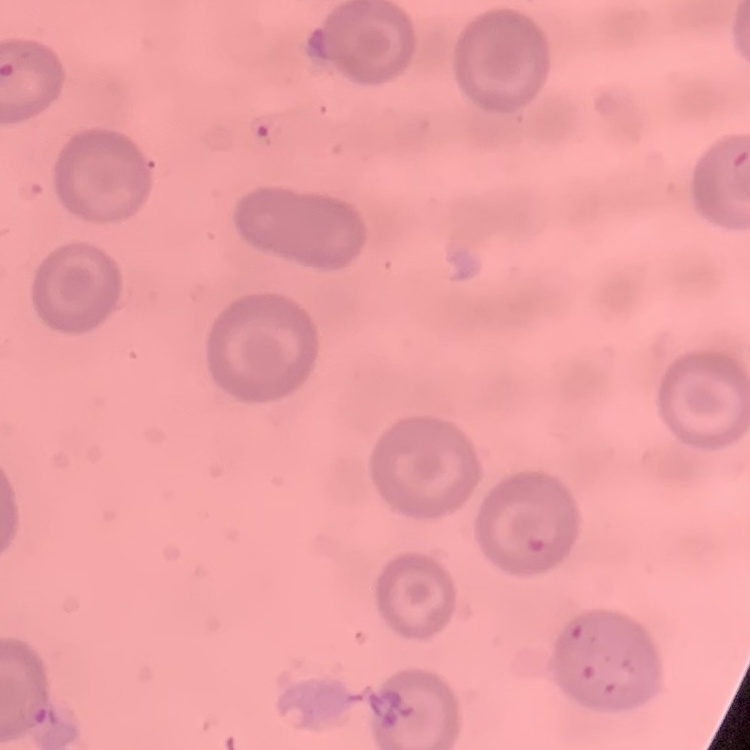

Summary:
  - Erythrocyte morphology: no rouleaux formation
  - Preparation: thin blood film
  - Image type: one tile cut from a larger photomicrograph
  - Stain: Field's or Giemsa